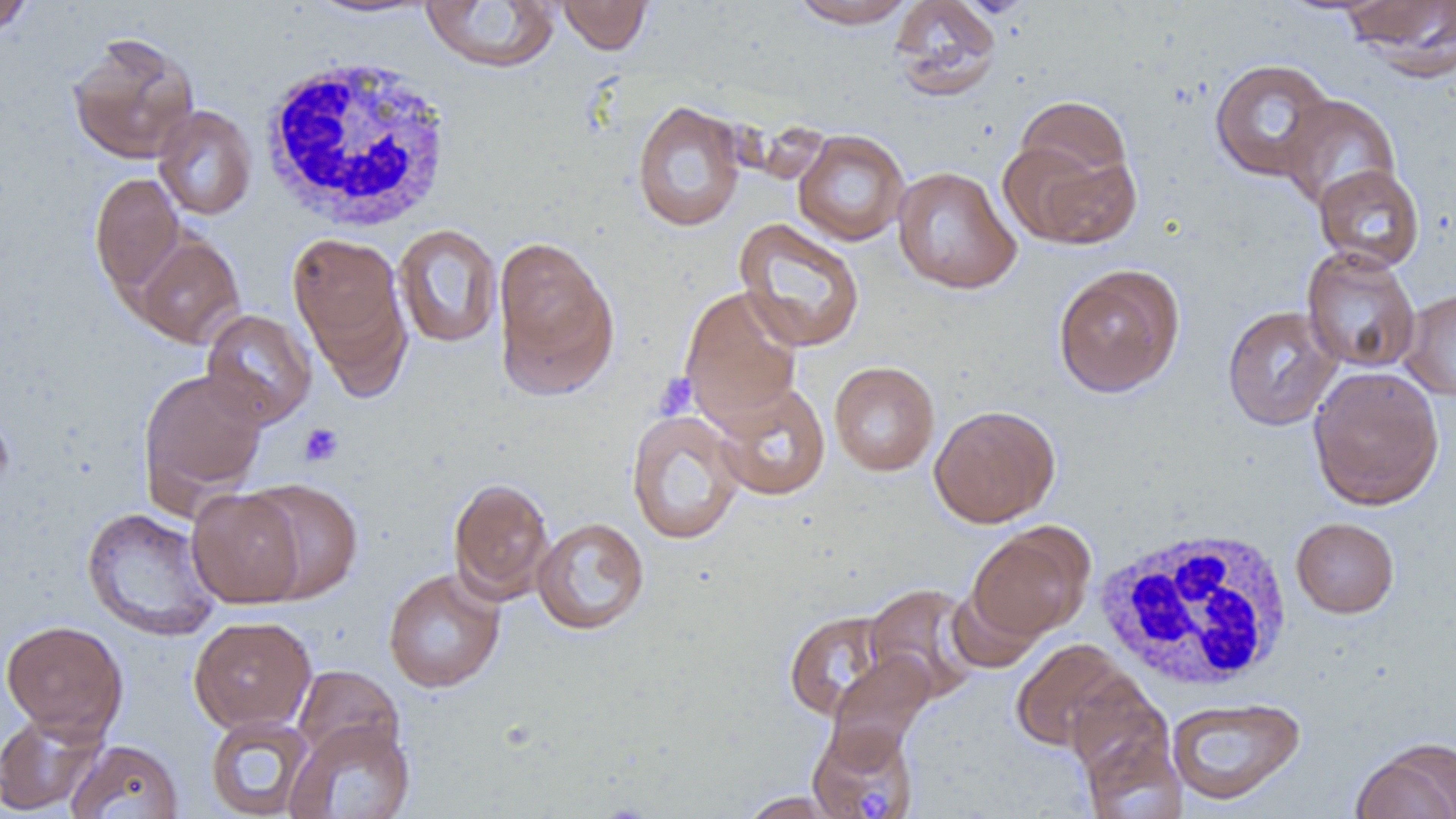

slide-level diagnosis = no evidence of blood parasites
image size = 1456×819 pixels
platelet locations = approximate bounding boxes as (x1, y1, x2, y2) in pixels: (654, 373, 698, 420), (298, 422, 345, 468)
field of view = single
magnification = 1000x
white blood cell locations = approximate bounding boxes as (x1, y1, x2, y2) in pixels: (257, 54, 458, 233), (1093, 527, 1294, 692)
modality = optical microscopy
uninfected red blood cell locations = approximate bounding boxes as (x1, y1, x2, y2) in pixels: (0, 0, 37, 38), (300, 0, 440, 20), (556, 0, 653, 55), (789, 0, 917, 29), (889, 0, 1003, 101), (1343, 0, 1455, 80), (419, 1, 561, 73), (66, 31, 200, 165), (1209, 58, 1337, 182), (1277, 93, 1401, 213), (1012, 94, 1134, 197), (631, 99, 747, 232), (153, 105, 257, 220), (792, 129, 910, 246), (1000, 131, 1141, 250), (1313, 164, 1425, 271), (892, 165, 1022, 294), (89, 172, 185, 297), (732, 218, 866, 353), (392, 223, 503, 349), (287, 233, 407, 369), (134, 234, 245, 348), (493, 236, 618, 396), (1301, 248, 1420, 373), (1052, 263, 1185, 398), (679, 286, 803, 427), (1400, 288, 1456, 400), (1222, 305, 1342, 431), (201, 308, 316, 428), (829, 361, 940, 476), (1308, 366, 1445, 511), (138, 368, 269, 506), (711, 381, 831, 501), (929, 404, 1061, 527), (626, 409, 746, 545), (447, 476, 555, 604), (240, 478, 364, 603), (187, 488, 306, 608), (81, 507, 222, 642), (532, 516, 650, 636), (1290, 517, 1399, 618), (968, 524, 1094, 641), (383, 567, 506, 693), (863, 583, 983, 703), (946, 583, 1045, 673), (782, 609, 902, 722), (188, 616, 316, 732), (1, 619, 128, 739), (1010, 640, 1133, 752), (825, 652, 936, 758), (292, 665, 403, 766), (1064, 676, 1175, 791), (1165, 696, 1306, 806), (0, 712, 105, 816), (205, 715, 314, 818), (285, 718, 416, 819), (807, 721, 920, 819), (1079, 730, 1187, 819), (66, 739, 183, 819), (1351, 739, 1456, 819), (736, 791, 846, 818)
preparation = thin blood smear